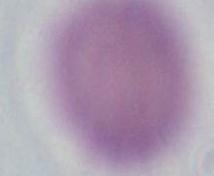
An erythrocyte is shown. 1000x magnification. Micrograph.